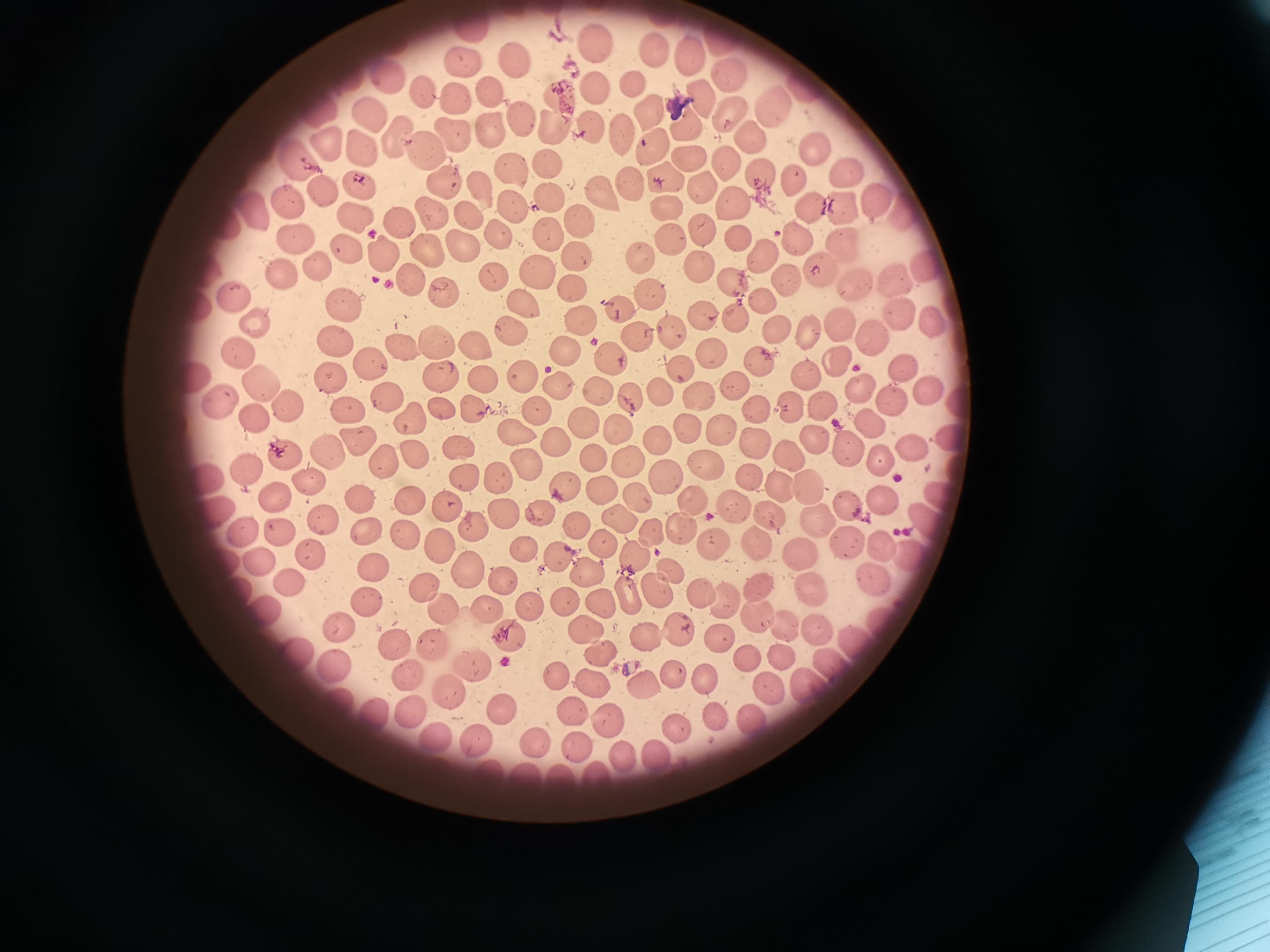
{
  "cell_locations": "approximate centers as {x, y} in pixels: {471, 30}, {723, 39}, {590, 40}, {652, 54}, {691, 55}, {460, 58}, {513, 58}, {729, 73}, {391, 76}, {595, 87}, {632, 87}, {492, 88}, {423, 92}, {559, 93}, {457, 98}, {704, 99}, {777, 106}, {734, 112}, {650, 113}, {366, 116}, {521, 118}, {557, 122}, {689, 124}, {490, 128}, {591, 128}, {455, 132}, {622, 133}, {396, 134}, {752, 136}, {325, 141}, {655, 144}, {427, 147}, {364, 148}, {813, 151}, {691, 155}, {294, 160}, {726, 160}, {548, 163}, {511, 171}, {847, 172}, {758, 174}, {792, 176}, {662, 178}, {440, 179}, {358, 182}, {701, 184}, {629, 185}, {478, 186}, {324, 187}, {548, 196}, {290, 198}, {601, 199}, {873, 201}, {513, 203}, {732, 206}, {839, 207}, {806, 208}, {666, 210}, {432, 211}, {357, 213}, {254, 214}, {907, 214}, {469, 217}, {578, 219}, {401, 223}, {501, 230}, {549, 231}, {705, 231}, {292, 235}, {670, 237}, {735, 240}, {798, 241}, {462, 243}, {428, 247}, {843, 247}, {349, 248}, {378, 254}, {578, 254}, {641, 257}, {764, 258}, {319, 265}, {700, 265}, {926, 265}, {533, 269}, {280, 272}, {818, 272}, {411, 276}, {493, 278}, {892, 278}, {735, 283}, {784, 283}, {575, 285}, {858, 286}, {442, 289}, {646, 290}, {237, 294}, {342, 302}, {758, 303}, {523, 305}, {619, 305}, {699, 316}, {736, 316}, {900, 316}, {578, 319}, {259, 324}, {840, 325}, {933, 326}, {779, 329}, {513, 331}, {672, 331}, {637, 334}, {811, 334}, {872, 338}, {334, 339}, {437, 340}, {475, 343}, {402, 347}, {568, 350}, {235, 352}, {709, 352}, {617, 354}, {372, 358}, {762, 359}, {843, 363}, {901, 366}, {683, 369}, {520, 372}, {806, 373}, {481, 378}, {328, 379}, {259, 383}, {556, 386}, {861, 387}, {736, 388}, {928, 390}, {603, 392}, {385, 393}, {658, 394}, {632, 398}, {702, 398}, {894, 402}, {219, 403}, {289, 403}, {789, 403}, {822, 404}, {346, 407}, {441, 407}, {471, 410}, {538, 410}, {755, 412}, {258, 417}, {405, 417}, {583, 420}, {872, 423}, {725, 426}, {517, 427}, {687, 428}, {658, 436}, {353, 440}, {556, 441}, {816, 441}, {752, 442}, {458, 445}, {911, 447}, {791, 450}, {851, 451}, {326, 452}, {417, 454}, {285, 455}, {591, 459}, {878, 461}, {527, 462}, {387, 463}, {705, 464}, {244, 470}, {466, 475}, {662, 475}, {210, 478}, {499, 478}, {313, 480}, {567, 484}, {781, 486}, {808, 489}, {275, 495}, {636, 495}, {357, 498}, {885, 499}, {405, 502}, {443, 503}, {692, 503}, {849, 505}, {734, 508}, {539, 509}, {503, 511}, {215, 514}, {769, 514}, {816, 520}, {621, 521}, {321, 522}, {576, 522}, {469, 524}, {930, 524}, {368, 528}, {656, 532}, {406, 534}, {244, 535}, {602, 541}, {846, 541}, {440, 544}, {712, 544}, {883, 546}, {760, 549}, {523, 550}, {635, 553}, {802, 553}, {313, 557}, {558, 557}, {909, 558}, {257, 564}, {380, 569}, {466, 569}, {589, 569}, {670, 572}, {500, 579}, {873, 579}, {290, 583}, {761, 584}, {806, 585}, {421, 587}, {656, 589}, {626, 593}, {702, 593}, {562, 598}, {599, 599}, {727, 600}, {365, 602}, {530, 605}, {443, 606}, {485, 608}, {266, 615}, {765, 617}, {587, 625}, {788, 627}, {676, 628}, {341, 629}, {393, 638}, {645, 638}, {721, 638}, {508, 641}, {431, 644}, {597, 651}, {296, 654}, {750, 657}, {778, 657}, {339, 662}, {473, 667}, {558, 671}, {408, 673}, {703, 674}, {593, 678}, {673, 678}, {646, 684}, {772, 690}, {448, 691}, {342, 700}, {569, 709}, {373, 710}, {413, 711}, {507, 713}, {605, 713}, {715, 717}, {747, 720}, {679, 726}, {431, 737}, {535, 742}, {580, 743}, {473, 744}, {662, 751}, {630, 756}, {599, 774}",
  "capture": "smartphone camera at the microscope eyepiece",
  "field_of_view": "single",
  "stain": "Giemsa",
  "preparation": "thin blood smear",
  "image_size": "1270×952 pixels"
}